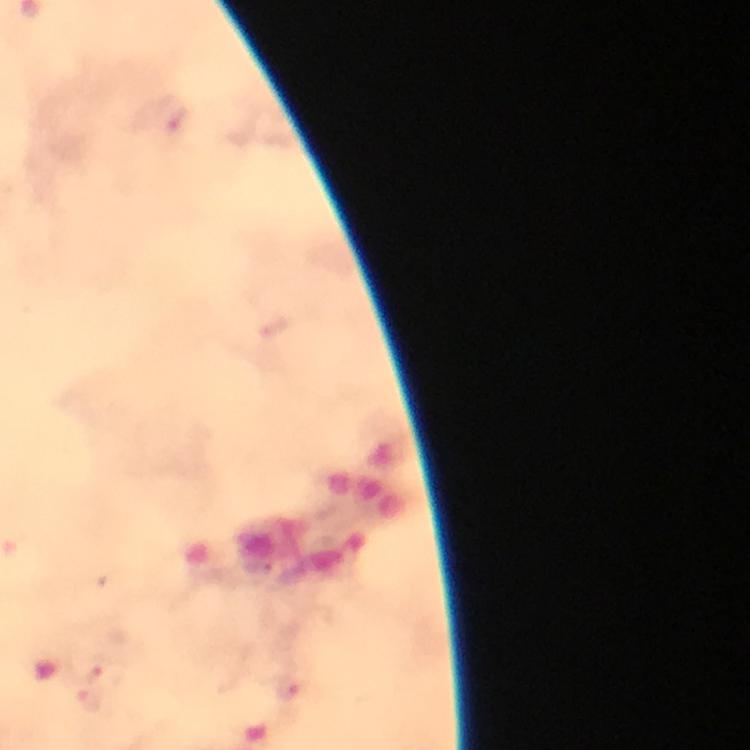

capture: smartphone camera through the microscope
magnification: 100x
context: from a diagnostic examination for malaria
stain: Giemsa
cropped_from: one field of view
plasmodium_parasite_locations: 'approximate centers as (x, y) in pixels: (173, 115), (102, 675), (287, 686), (89, 700)'
immersion_oil: applied
preparation: thick smear
image_size: 750×750 pixels